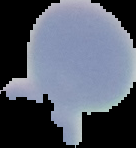
{
  "preparation": "thin blood film",
  "result": "no malaria parasites detected",
  "image_type": "cell region segmented out of the field of view; surrounding area masked to black",
  "image_size": "136×148 pixels"
}